Assess the morphology of the erythrocytes.
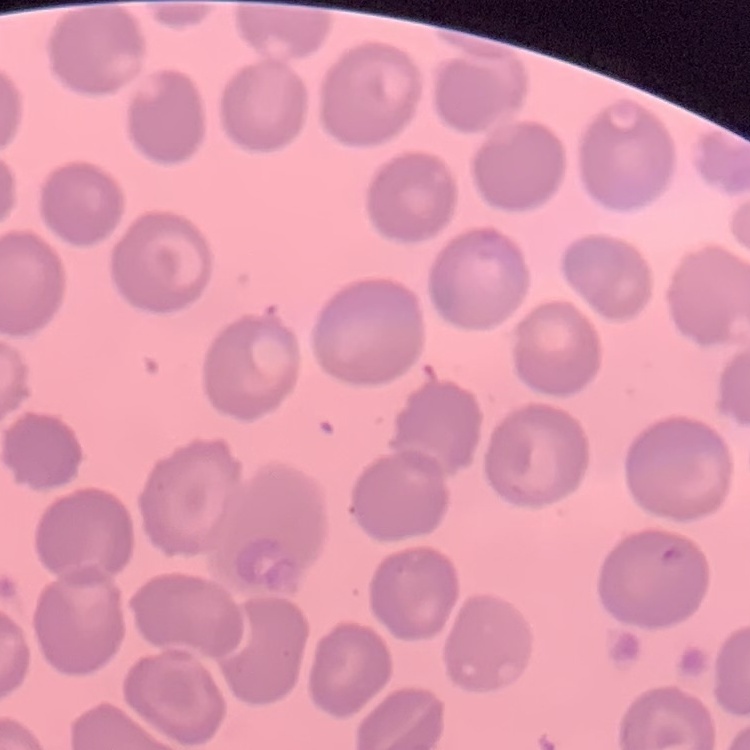
No rouleaux formation.

Stained with either Field's or Giemsa. One tile cut from a larger photomicrograph. Thin blood smear.